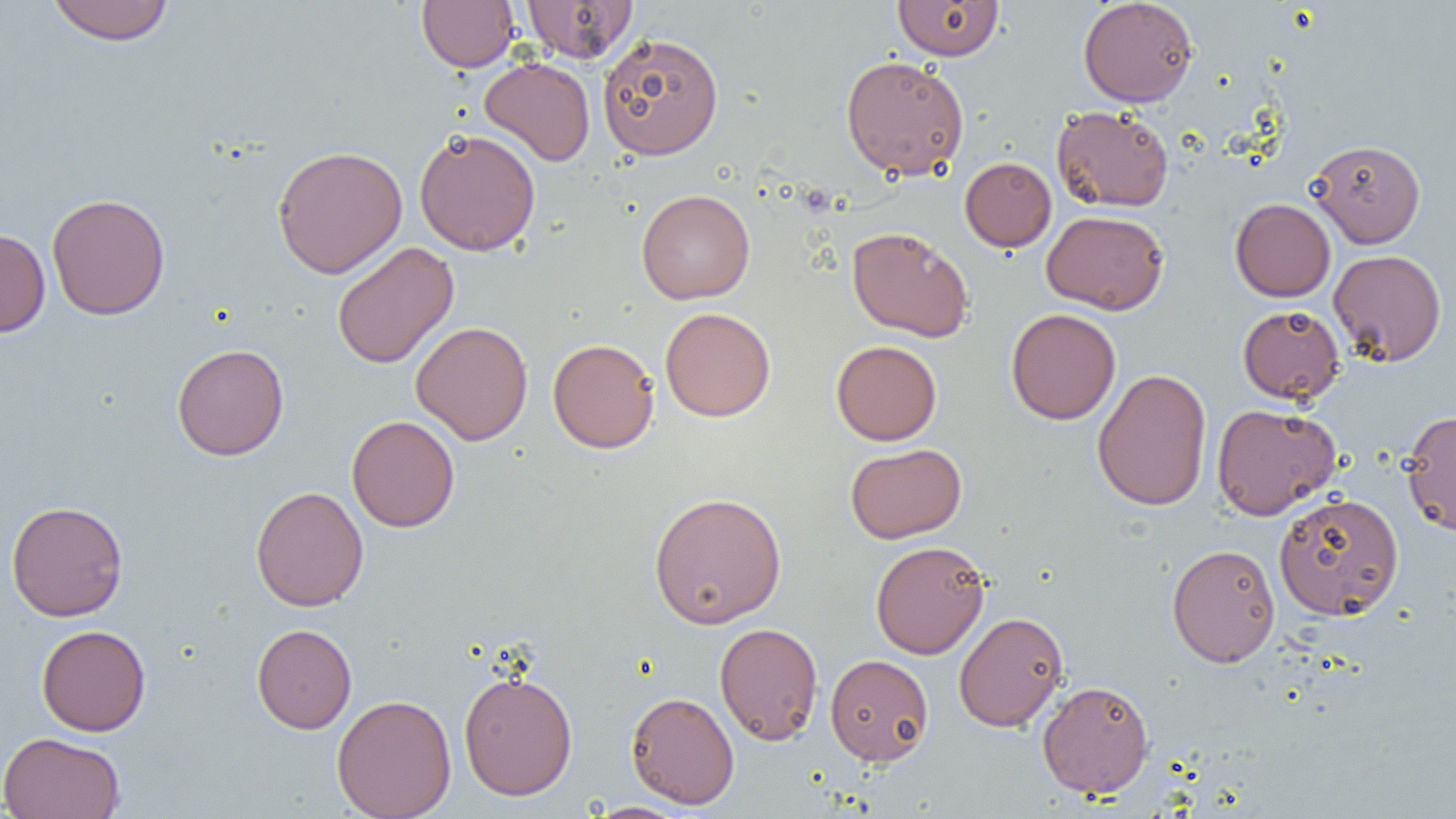

Approximate bounding boxes as (x1, y1, x2, y2) in pixels. Uninfected red blood cell locations: (46, 0, 175, 45), (417, 0, 519, 72), (522, 0, 637, 63), (892, 0, 1004, 61), (1078, 0, 1198, 107), (597, 32, 724, 160), (840, 55, 969, 180), (480, 57, 595, 165), (1051, 105, 1175, 212), (414, 128, 541, 256), (1307, 139, 1426, 248), (272, 145, 408, 278), (960, 157, 1056, 251), (636, 189, 755, 304), (47, 193, 170, 320), (1230, 198, 1336, 301), (1042, 210, 1169, 314), (846, 226, 974, 342), (0, 227, 50, 337), (332, 241, 459, 369), (1329, 249, 1447, 366), (1237, 304, 1345, 405), (660, 307, 775, 422), (1006, 308, 1121, 424), (411, 321, 533, 445), (547, 338, 659, 453), (831, 340, 942, 445), (172, 343, 289, 460), (1092, 368, 1212, 511), (1211, 403, 1341, 520), (1401, 410, 1456, 536), (346, 415, 460, 532), (845, 442, 967, 543), (250, 486, 368, 611), (648, 491, 786, 629), (1273, 491, 1404, 619), (6, 500, 128, 621), (870, 540, 989, 659), (1167, 543, 1280, 667), (954, 611, 1068, 732), (714, 622, 824, 745), (252, 623, 357, 734), (36, 624, 150, 735), (825, 653, 934, 765), (458, 670, 578, 800), (1037, 680, 1154, 798), (626, 691, 739, 809), (332, 694, 457, 819), (0, 731, 126, 819), (585, 802, 692, 818). Slide-level diagnosis: negative for blood parasites. Thin blood film. One field of a larger specimen. Captured at 1000x magnification. Image is 1456×819 pixels. Light microscopy.